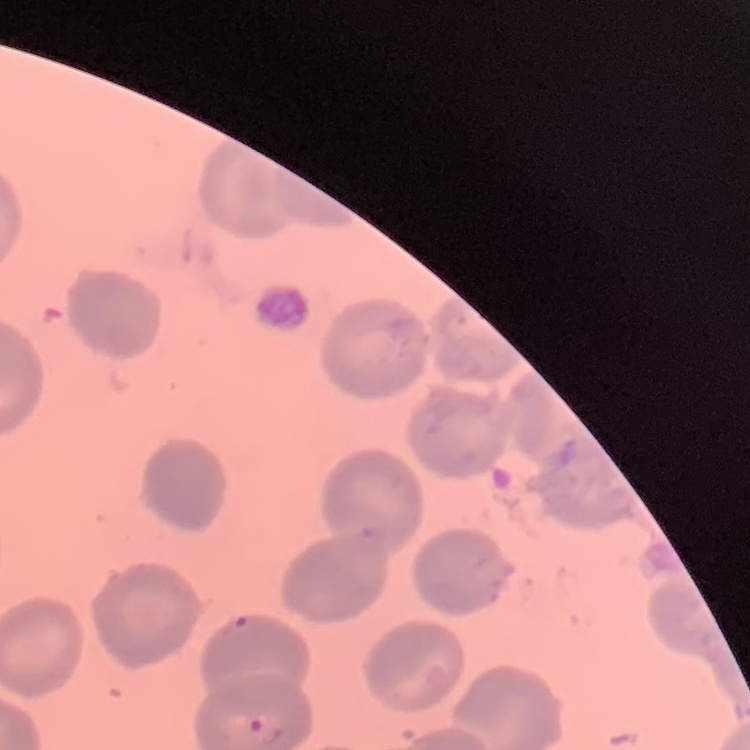

The erythrocytes exhibit no rouleaux formation. Thin blood smear. Square crop of a larger photomicrograph. Stained with either Field's or Giemsa.